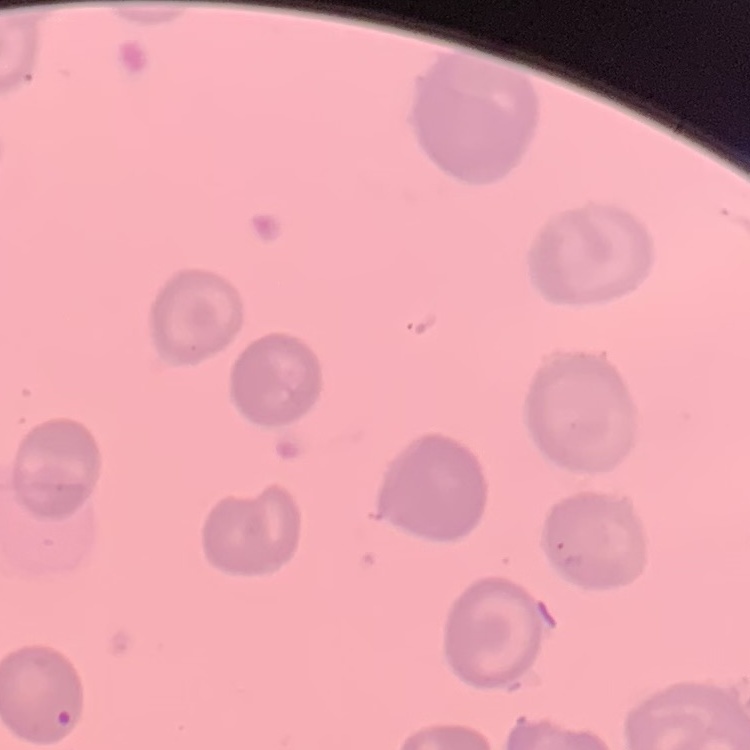

erythrocyte_morphology: no rouleaux formation
image_type: one tile cut from a larger photomicrograph
preparation: thin blood film
stain: Field's or Giemsa